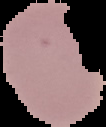

Malaria status: uninfected. Cell region segmented out of the field of view; the surrounding area is masked to black. From a thin blood smear. Image is 106×127 pixels.